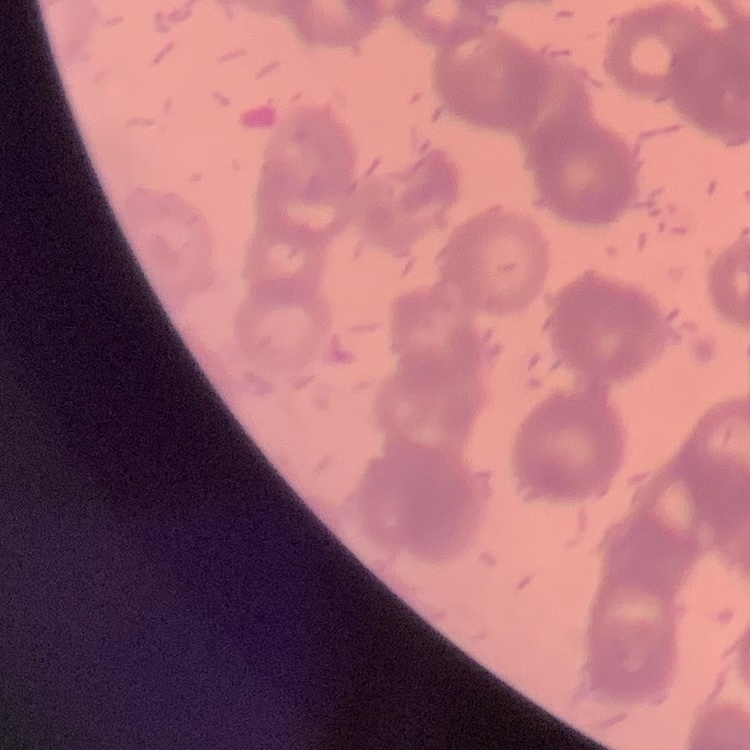 The red blood cells show rouleaux formation. Thin blood smear. Stained with either Field's or Giemsa. Square crop of a larger photomicrograph.